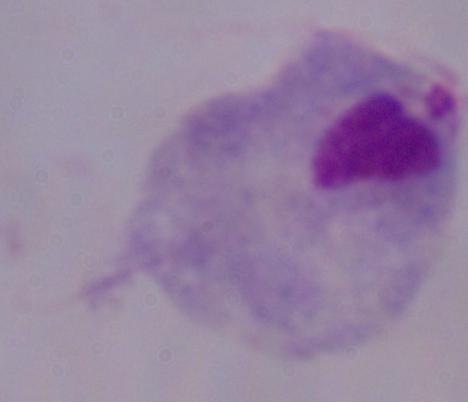

A trichomonad is shown. Captured at 1000x magnification. Photomicrograph.